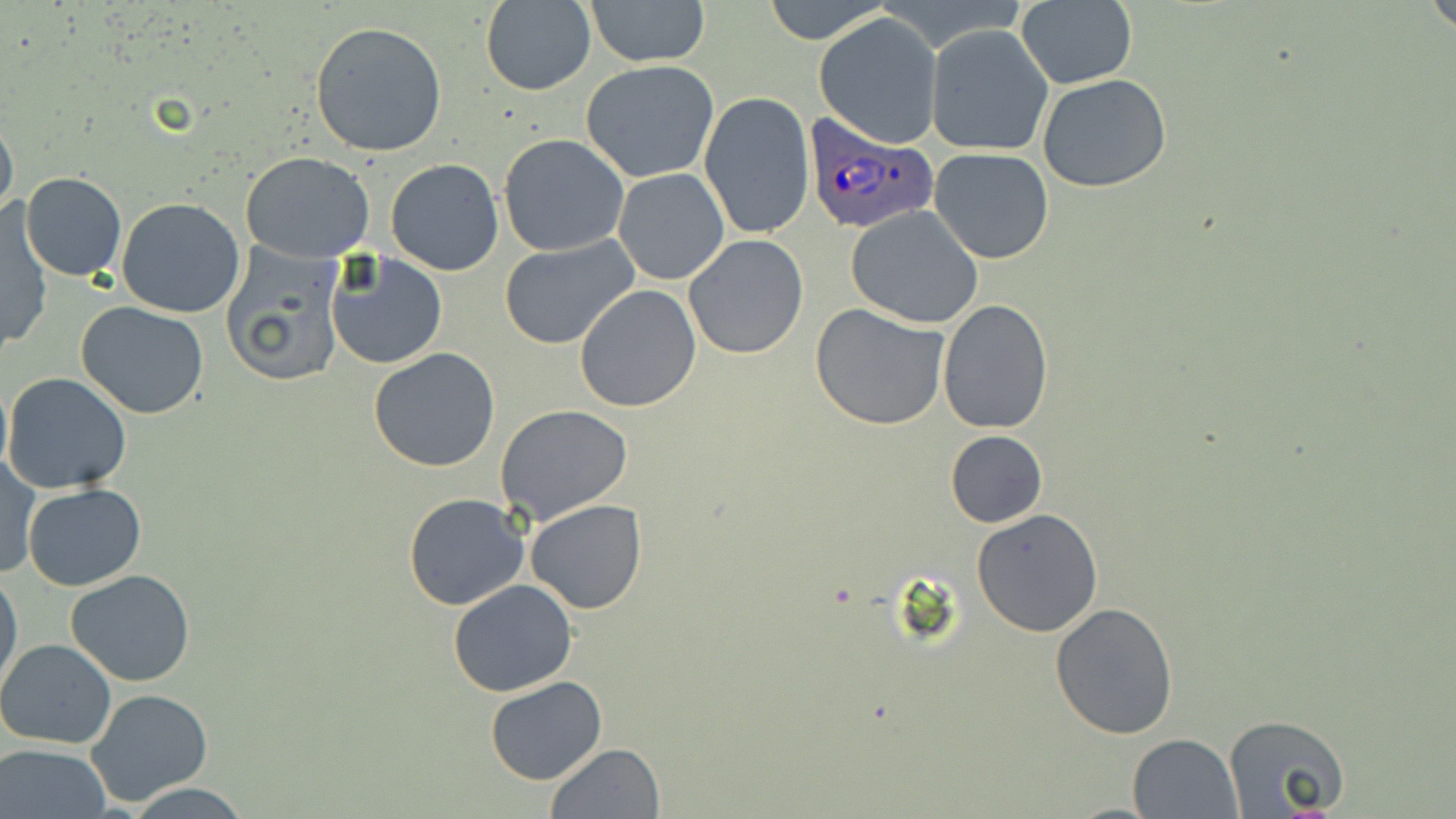
slide_level_diagnosis: Plasmodium ovale
magnification: 1000x
stain: May-Grünwald-Giemsa
modality: light microscopy
uninfected_red_blood_cell_locations: 'approximate bounding boxes as [x1, y1, x2, y2] in pixels: [585, 0, 711, 67], [756, 0, 892, 45], [1426, 0, 1456, 35], [481, 1, 596, 95], [1015, 1, 1137, 88], [814, 13, 942, 147], [310, 21, 447, 158], [926, 25, 1053, 158], [581, 60, 719, 182], [1036, 73, 1173, 192], [699, 92, 815, 240], [0, 114, 19, 225], [498, 133, 629, 256], [928, 148, 1055, 263], [242, 151, 375, 262], [386, 158, 504, 276], [613, 168, 729, 284], [19, 171, 127, 280], [116, 198, 246, 319], [846, 205, 984, 329], [2, 207, 51, 354], [499, 234, 641, 350], [683, 236, 808, 359], [222, 247, 346, 387], [325, 253, 447, 370], [574, 283, 703, 413], [937, 299, 1053, 434], [77, 302, 209, 419], [809, 302, 952, 431], [368, 348, 500, 471], [3, 372, 132, 494], [496, 404, 634, 525], [946, 431, 1047, 528], [1, 456, 39, 579], [22, 484, 148, 591], [402, 491, 530, 611], [524, 500, 648, 615], [972, 509, 1104, 637], [0, 567, 22, 695], [65, 569, 196, 687], [446, 579, 578, 697], [1050, 602, 1180, 740], [0, 638, 119, 749], [483, 677, 607, 786], [84, 688, 213, 808], [1223, 713, 1350, 815], [1127, 732, 1241, 817], [544, 742, 666, 819], [0, 745, 114, 819], [124, 784, 252, 817]'
image_size: 1456×819 pixels
preparation: thin blood smear
field_of_view: single
plasmodium_ovale_infected_red_blood_cell_locations: 'approximate bounding boxes as [x1, y1, x2, y2] in pixels: [803, 114, 941, 235]'